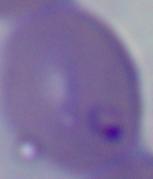

Summary:
  - Magnification: 1000x
  - Modality: photomicrograph
  - Identification: Babesia